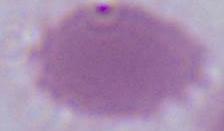

identification: erythrocyte
modality: micrograph
magnification: 1000x